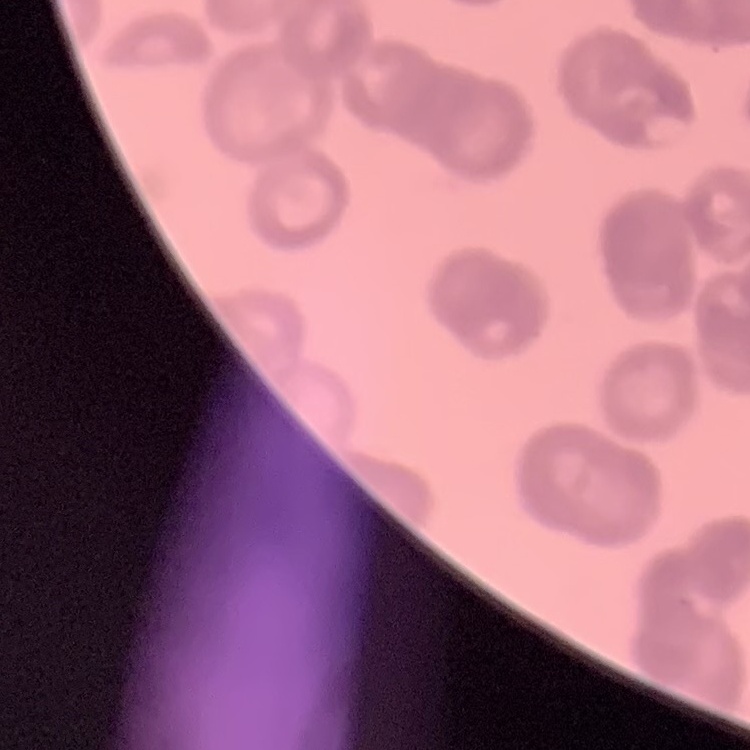
{
  "red_blood_cell_morphology": "rouleaux formation",
  "stain": "Field's or Giemsa",
  "preparation": "thin peripheral smear",
  "image_type": "one tile cut from a larger photomicrograph"
}